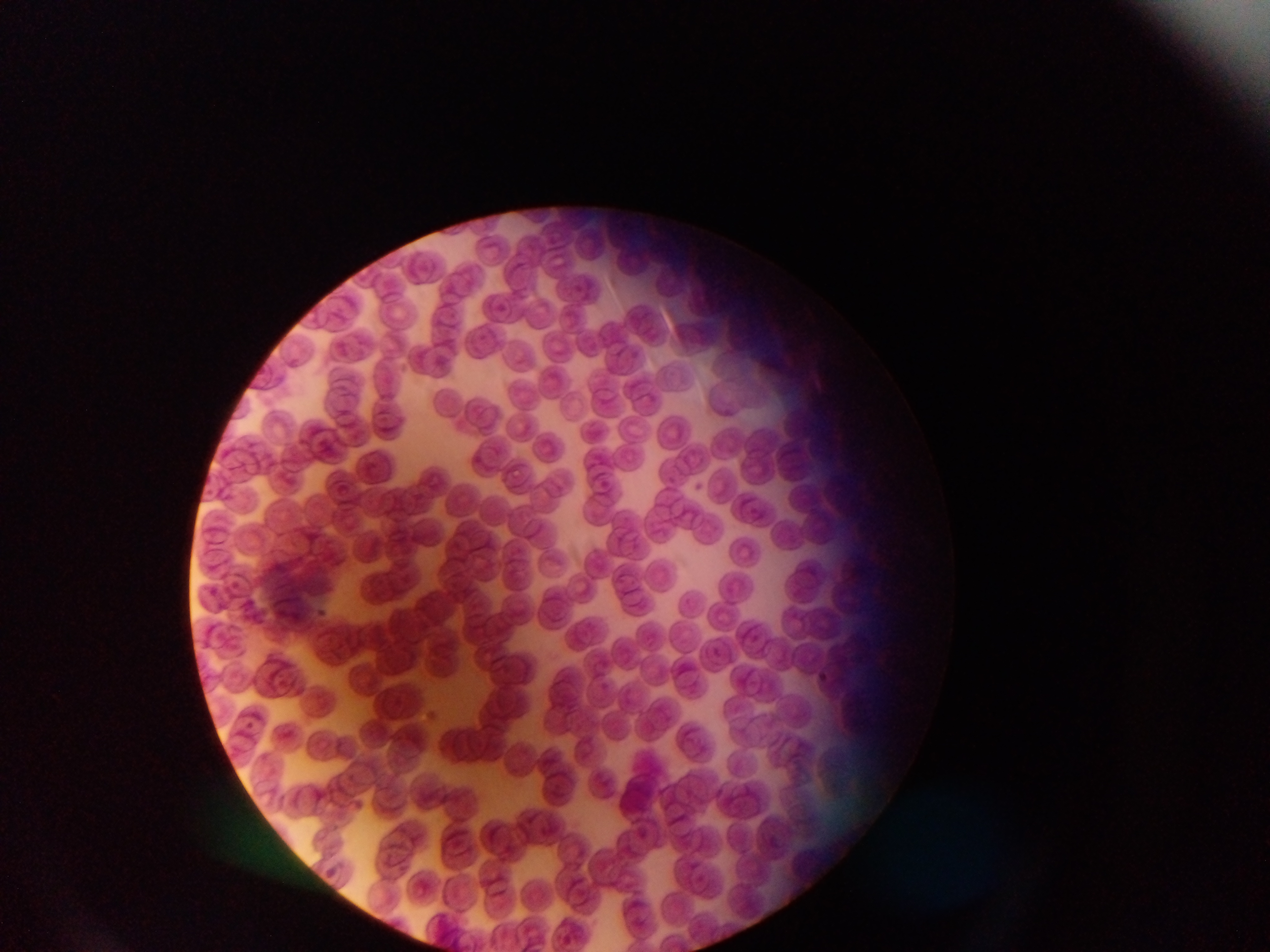

image size = 1270×952 pixels
field of view = single
preparation = thin blood film
country = Ghana
leukocyte locations = approximate bounding boxes as [left, top, right, bottom] in pixels: [354, 445, 398, 490]
capture = mobile-phone photograph through a microscope